Identify the parasite.
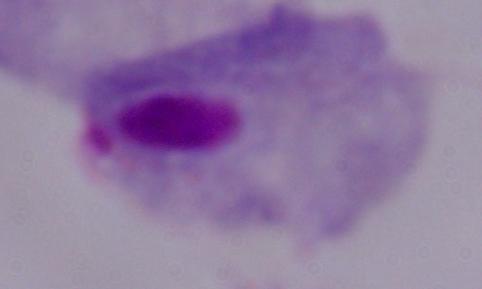

A trichomonad.

1000x magnification. Micrograph.